Outline each blood parasite and name the species.
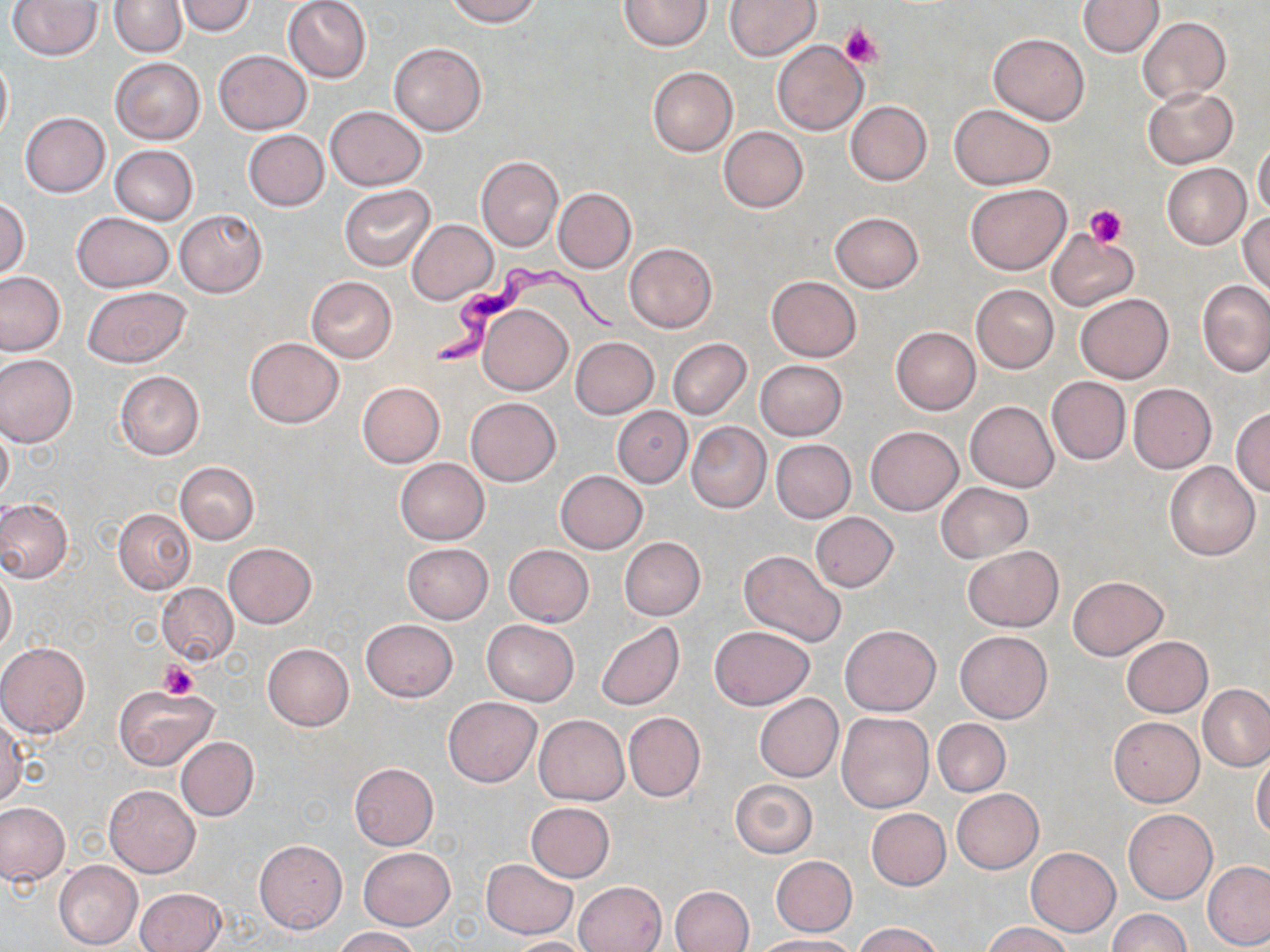

Approximate bounding boxes as (x1,y1)-(x2,y2) corner pairs in pixels.
Trypanosoma brucei: (432,266)-(625,366).
No Plasmodium falciparum, Plasmodium ovale, Plasmodium malariae, Plasmodium vivax, or Babesia divergens observed.

Summary:
  - Platelet locations: (840,23)-(882,69), (1084,204)-(1128,248), (159,661)-(197,701)
  - Uninfected red blood cell locations: (282,0)-(372,83), (444,0)-(542,26), (619,0)-(713,51), (724,0)-(822,61), (1078,0)-(1163,57), (7,1)-(102,60), (111,1)-(187,57), (174,1)-(257,37), (1137,17)-(1230,104), (989,32)-(1089,125), (771,40)-(868,134), (390,42)-(486,136), (212,50)-(312,134), (0,52)-(12,144), (109,57)-(205,145), (647,66)-(739,156), (1144,86)-(1237,168), (846,102)-(931,184), (325,105)-(426,191), (949,105)-(1057,190), (20,112)-(110,197), (719,126)-(808,213), (244,130)-(328,211), (1251,139)-(1270,218), (109,145)-(199,225), (476,155)-(562,251), (1163,164)-(1250,248), (340,183)-(436,272), (965,183)-(1071,275), (552,188)-(636,273), (0,198)-(30,280), (175,209)-(267,296), (72,212)-(173,293), (830,212)-(923,293), (1238,213)-(1270,297), (407,218)-(497,305), (1046,231)-(1138,311), (624,242)-(717,334), (0,271)-(68,358), (306,276)-(397,364), (766,276)-(860,362), (1198,280)-(1270,376), (972,284)-(1059,374), (82,286)-(190,368), (1075,293)-(1173,384), (478,304)-(571,394), (891,326)-(980,414), (245,337)-(344,428), (570,337)-(659,418), (668,339)-(751,419), (0,354)-(78,447), (754,359)-(847,441), (114,370)-(204,461), (1046,376)-(1131,465), (357,382)-(445,468), (1128,384)-(1216,472), (466,397)-(560,485), (965,401)-(1059,492), (1231,405)-(1270,497), (612,406)-(692,486), (0,420)-(14,505), (686,421)-(772,513), (865,425)-(963,516), (772,439)-(856,522), (394,458)-(490,545), (1164,461)-(1260,561), (174,462)-(260,544), (555,470)-(648,554), (937,482)-(1032,562), (0,499)-(73,584), (114,508)-(195,595), (811,512)-(897,591), (619,536)-(706,620), (224,543)-(316,628), (402,543)-(493,624), (503,544)-(594,626), (963,545)-(1063,631), (738,550)-(846,648), (0,567)-(17,657), (1067,576)-(1167,659), (156,583)-(237,664), (360,619)-(457,702), (483,620)-(579,705), (596,622)-(684,711), (840,624)-(940,716), (710,625)-(816,709), (955,630)-(1052,723), (1122,636)-(1212,717), (0,643)-(90,738), (262,643)-(354,731), (1198,685)-(1270,770), (113,686)-(218,770), (754,693)-(843,782), (444,697)-(542,787), (623,712)-(705,802), (835,712)-(934,814), (0,713)-(25,807), (534,715)-(630,804), (1108,717)-(1204,806), (932,718)-(1011,796), (175,737)-(258,820), (1251,754)-(1270,840), (349,763)-(438,849), (729,779)-(817,858), (105,785)-(200,877), (951,788)-(1043,874), (526,802)-(614,881), (0,803)-(68,885), (867,808)-(950,890), (1123,808)-(1217,905), (254,840)-(347,933), (358,847)-(456,930), (1025,847)-(1121,936), (771,855)-(856,935), (481,859)-(577,937), (1203,860)-(1270,951), (53,861)-(142,949), (574,881)-(667,952), (670,885)-(754,952), (136,887)-(226,952), (1107,909)-(1189,952), (853,923)-(946,952), (983,923)-(1074,952), (331,927)-(422,951), (752,935)-(855,952), (504,936)-(595,952)
  - Slide-level diagnosis: Trypanosoma brucei
  - Preparation: thin blood smear
  - Modality: optical microscopy
  - Stain: May-Grünwald-Giemsa
  - Image size: 1270×952 pixels
  - Field of view: one of a larger specimen
  - Magnification: 1000x